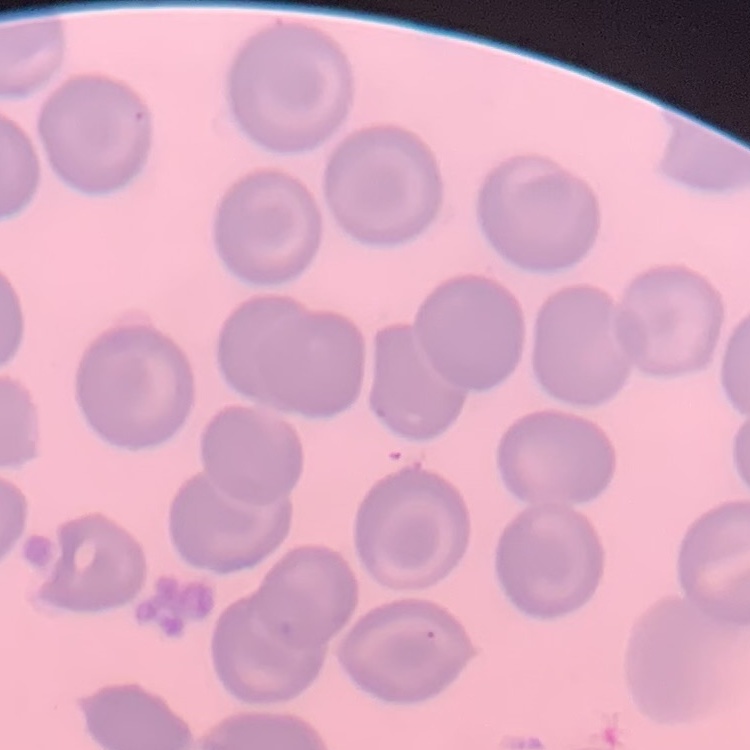
The red blood cells exhibit no rouleaux formation. Stained with either Field's or Giemsa. One tile cut from a larger photomicrograph. Thin peripheral smear.